Describe the morphology of the red blood cells.
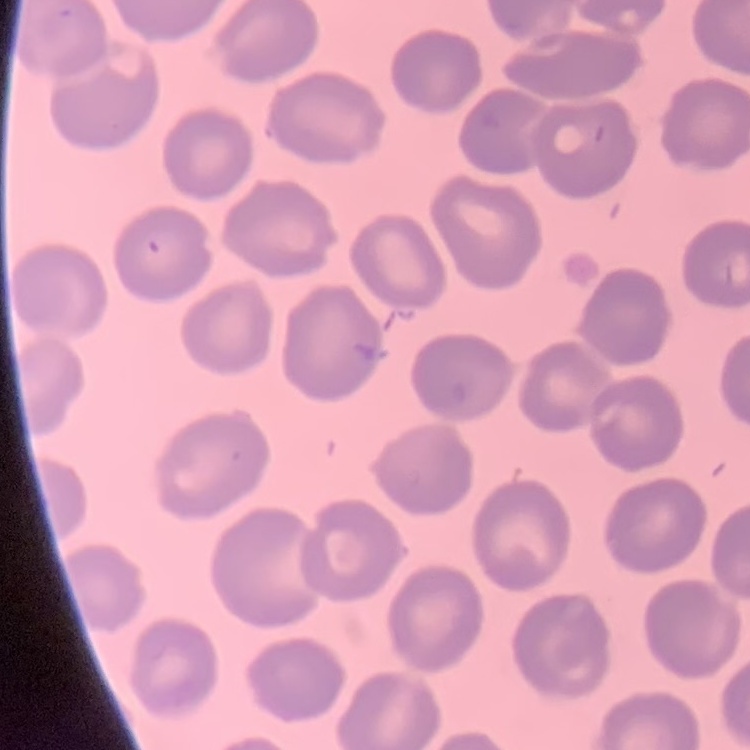
They show no rouleaux formation.

One tile cut from a larger photomicrograph. Thin blood smear. Stained with either Field's or Giemsa.